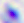
Toxoplasma gondii is seen. 400x magnification. Photomicrograph.